Report the malaria status of this cell.
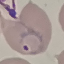

It is parasitized.

capture = smartphone through the microscope eyepiece
image type = automatically extracted cell patch, resized to 64 × 64 pixels
preparation = thin blood film
stain = Giemsa